Locate every uninfected red blood cell.
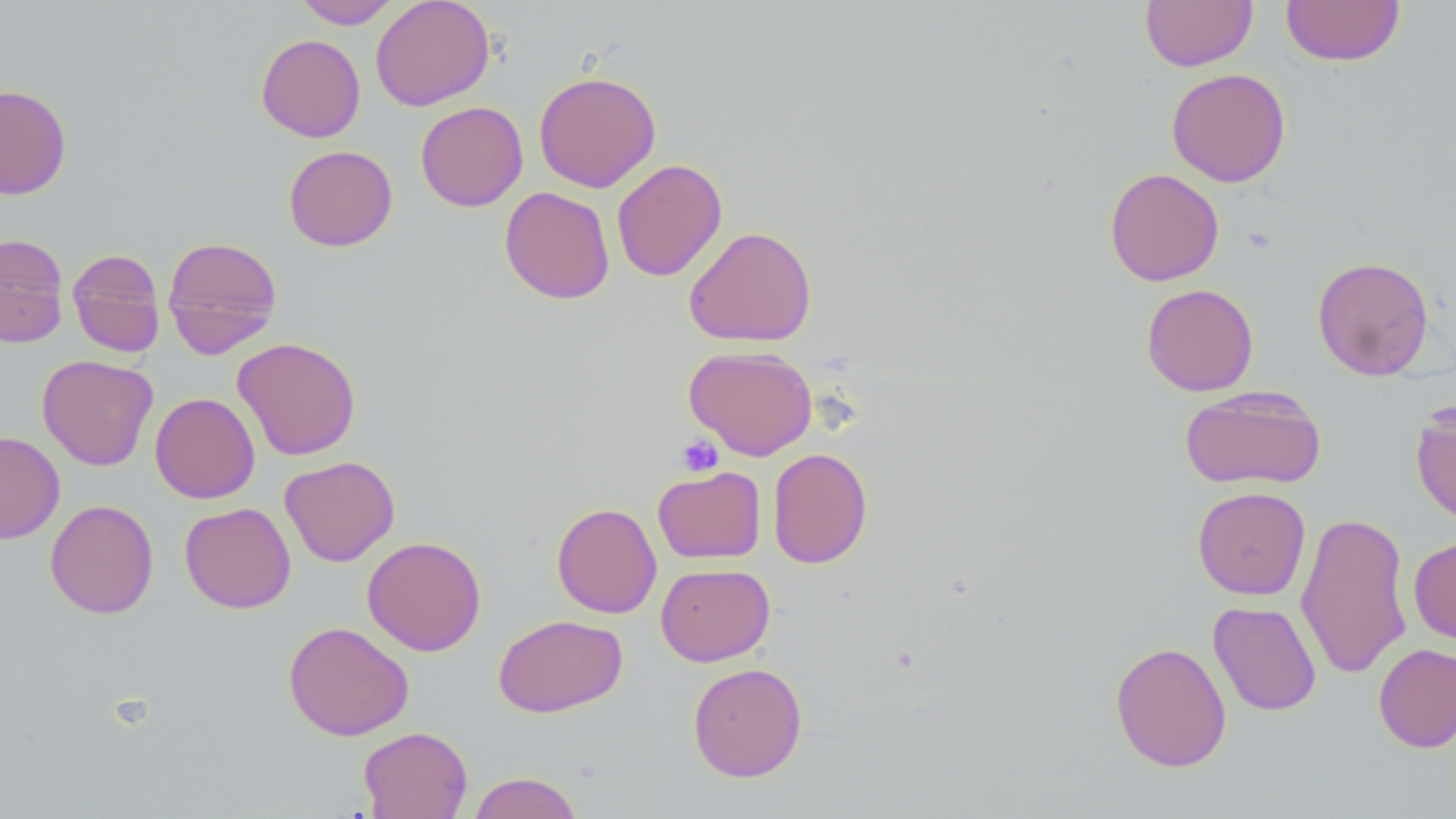
Approximate bounding boxes as (x1,y1)-(x2,y2) corner pairs in pixels.
Uninfected red blood cells: (293,0)-(401,29), (371,0)-(495,111), (1140,0)-(1257,71), (1281,0)-(1405,66), (256,34)-(365,142), (1166,68)-(1291,187), (533,71)-(661,193), (0,84)-(72,199), (415,101)-(528,211), (283,145)-(398,251), (612,159)-(727,281), (1104,168)-(1225,286), (499,186)-(615,305), (683,225)-(817,347), (0,233)-(69,347), (162,236)-(283,357), (67,248)-(166,357), (1312,256)-(1435,381), (1141,283)-(1259,396), (233,337)-(361,460), (683,345)-(817,460), (37,354)-(158,470), (1179,385)-(1327,490), (150,392)-(260,504), (1410,401)-(1456,528), (0,431)-(65,543), (768,447)-(873,569), (280,456)-(400,566), (653,465)-(766,563), (1192,486)-(1311,600), (44,499)-(159,618), (179,502)-(296,613), (551,502)-(662,618), (1296,510)-(1413,680), (362,536)-(487,656), (1409,536)-(1456,645), (655,563)-(775,667), (1207,601)-(1322,716), (493,613)-(628,717), (283,621)-(414,741), (1110,641)-(1232,772), (1373,643)-(1456,753), (687,662)-(807,781), (358,726)-(472,818), (467,771)-(583,819).

Summary:
  - Platelet locations: (676,434)-(723,477)
  - Slide-level diagnosis: no evidence of blood parasites
  - Image size: 1456×819 pixels
  - Magnification: 1000x
  - Field of view: one of a larger specimen
  - Stain: May-Grünwald-Giemsa
  - Modality: light microscopy
  - Preparation: thin blood smear